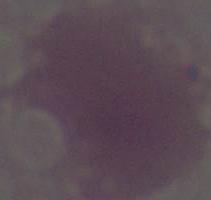

modality = photomicrograph
magnification = 1000x
identification = erythrocyte